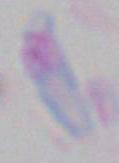
Summary:
  - Identification: Toxoplasma gondii
  - Modality: photomicrograph
  - Magnification: 1000x